Identify the blood parasite species.
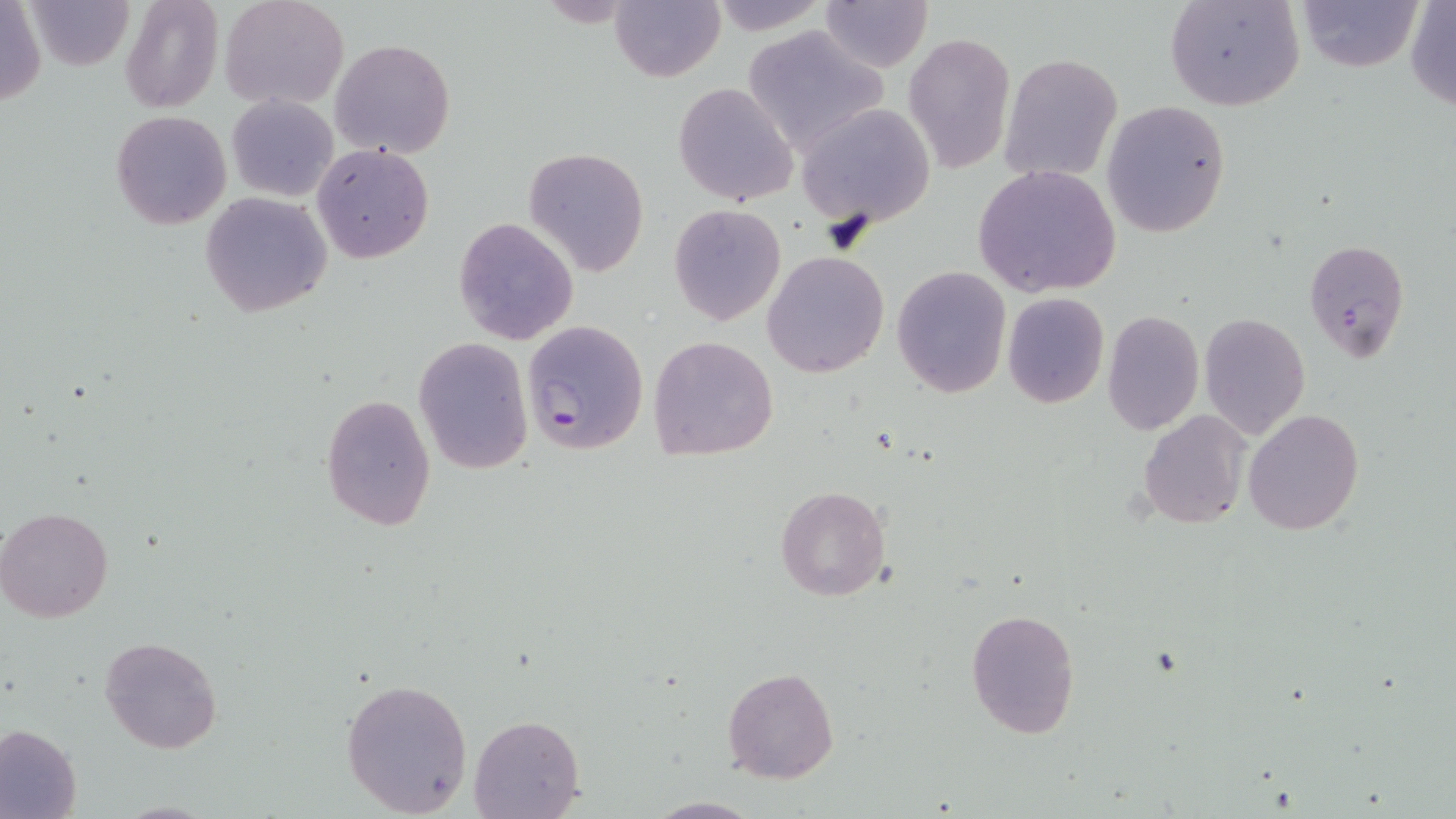
Plasmodium falciparum.

preparation: thin blood film
uninfected_red_blood_cell_locations: 'approximate bounding boxes as named x1/y1/x2/y2 corners in pixels: (x1=1, y1=0, x2=46, y2=106), (x1=218, y1=0, x2=349, y2=111), (x1=707, y1=0, x2=830, y2=35), (x1=821, y1=0, x2=933, y2=72), (x1=1163, y1=0, x2=1306, y2=112), (x1=1296, y1=0, x2=1422, y2=74), (x1=29, y1=1, x2=133, y2=69), (x1=120, y1=1, x2=223, y2=113), (x1=611, y1=1, x2=723, y2=82), (x1=1405, y1=1, x2=1456, y2=109), (x1=741, y1=24, x2=886, y2=155), (x1=902, y1=31, x2=1014, y2=177), (x1=328, y1=38, x2=455, y2=158), (x1=999, y1=53, x2=1124, y2=183), (x1=673, y1=81, x2=798, y2=206), (x1=227, y1=95, x2=338, y2=200), (x1=1101, y1=100, x2=1233, y2=238), (x1=797, y1=104, x2=936, y2=228), (x1=111, y1=111, x2=232, y2=229), (x1=311, y1=143, x2=435, y2=263), (x1=523, y1=146, x2=648, y2=277), (x1=972, y1=164, x2=1121, y2=299), (x1=199, y1=191, x2=332, y2=315), (x1=668, y1=204, x2=784, y2=327), (x1=452, y1=217, x2=578, y2=345), (x1=762, y1=250, x2=889, y2=378), (x1=892, y1=266, x2=1012, y2=398), (x1=1003, y1=293, x2=1110, y2=409), (x1=1102, y1=309, x2=1204, y2=437), (x1=1198, y1=313, x2=1310, y2=438), (x1=413, y1=335, x2=534, y2=475), (x1=649, y1=335, x2=779, y2=462), (x1=318, y1=393, x2=436, y2=531), (x1=1243, y1=409, x2=1364, y2=534), (x1=1137, y1=411, x2=1250, y2=528), (x1=775, y1=486, x2=889, y2=602), (x1=1, y1=505, x2=116, y2=623), (x1=965, y1=607, x2=1081, y2=739), (x1=100, y1=636, x2=222, y2=754), (x1=721, y1=667, x2=839, y2=784), (x1=341, y1=678, x2=473, y2=816), (x1=468, y1=715, x2=584, y2=819), (x1=0, y1=722, x2=82, y2=819), (x1=642, y1=796, x2=765, y2=818)'
modality: optical microscopy
magnification: 1000x
stain: May-Grünwald-Giemsa
field_of_view: one of a larger specimen
plasmodium_falciparum_infected_red_blood_cell_locations: 'approximate bounding boxes as named x1/y1/x2/y2 corners in pixels: (x1=1305, y1=238, x2=1409, y2=362), (x1=521, y1=320, x2=650, y2=454)'
image_size: 1456×819 pixels